Describe the morphology of the erythrocytes.
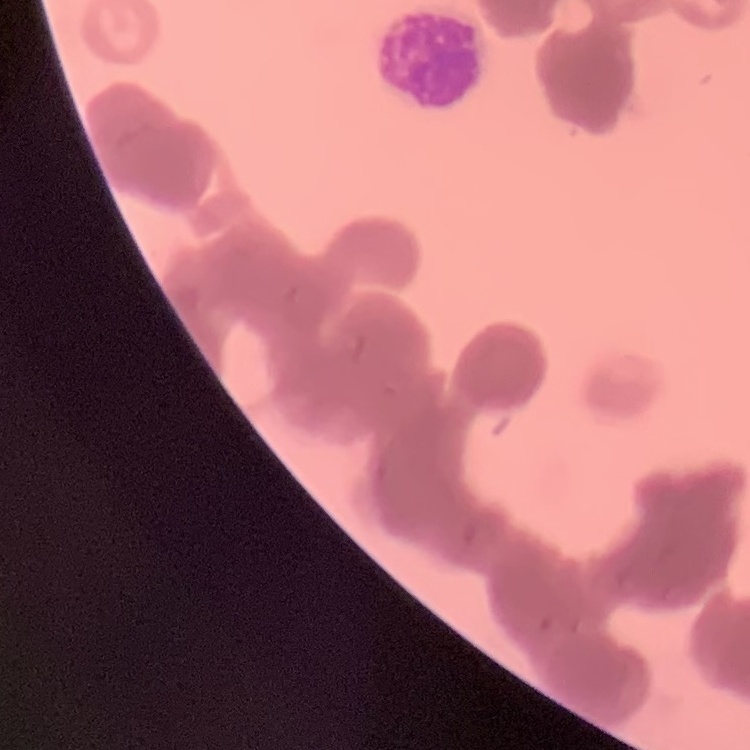

They show rouleaux formation.

Summary:
  - Stain: Field's or Giemsa
  - Image type: one tile cut from a larger photomicrograph
  - Preparation: thin blood film